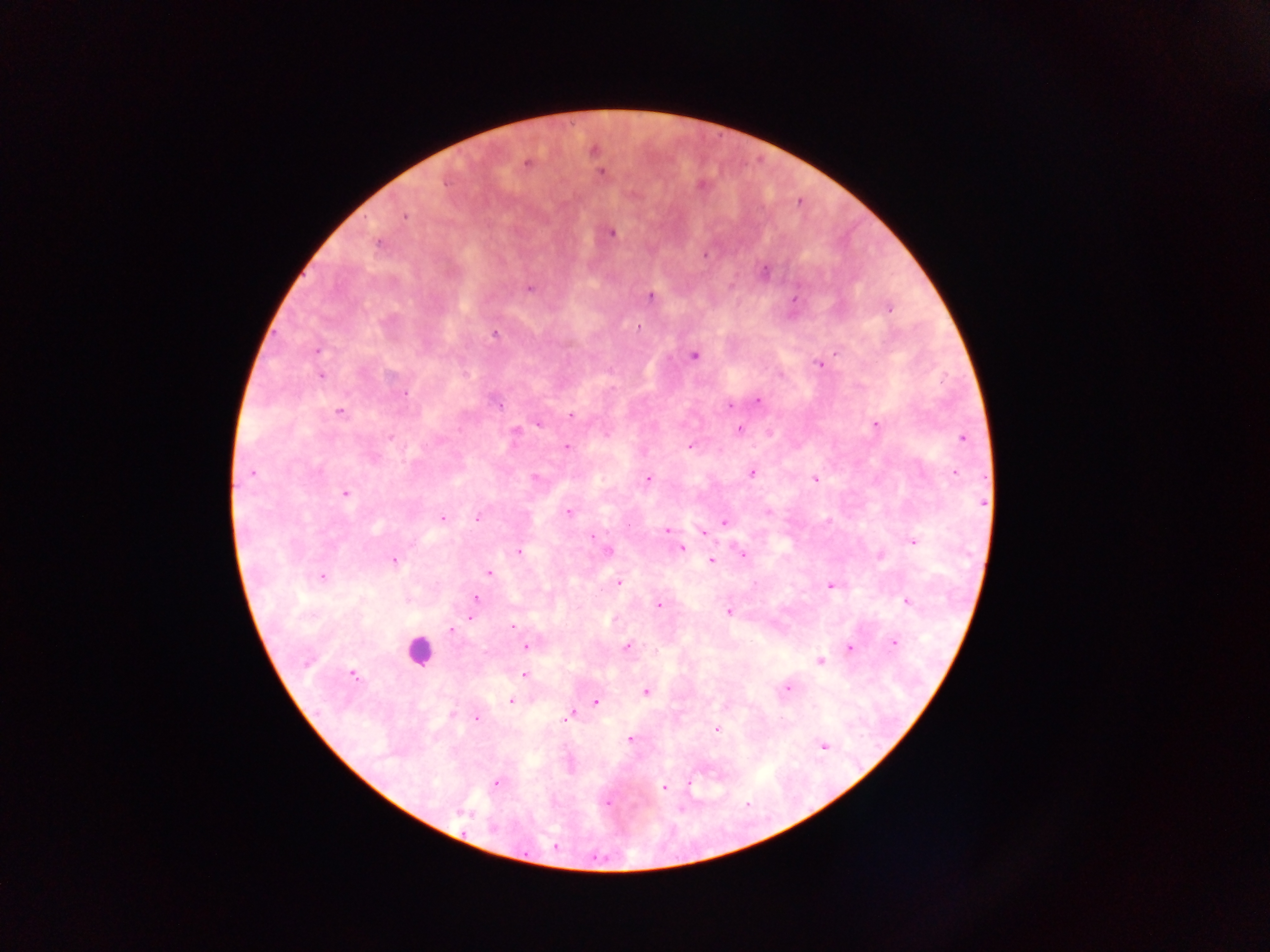
Approximate centers as {x, y} in pixels.
Summary:
  - Leukocyte locations: {420, 650}
  - Plasmodium parasite locations: {593, 150}, {527, 163}, {602, 174}, {405, 216}, {611, 233}, {377, 244}, {704, 255}, {765, 271}, {529, 288}, {650, 296}, {794, 299}, {890, 308}, {638, 327}, {495, 334}, {316, 350}, {837, 353}, {694, 355}, {826, 360}, {820, 364}, {320, 375}, {780, 375}, {404, 394}, {757, 401}, {498, 405}, {730, 406}, {339, 413}, {570, 415}, {538, 423}, {876, 425}, {739, 429}, {390, 437}, {962, 439}, {566, 446}, {690, 446}, {752, 473}, {251, 474}, {956, 474}, {535, 477}, {648, 479}, {815, 479}, {345, 494}, {568, 512}, {478, 517}, {443, 518}, {724, 522}, {667, 530}, {703, 532}, {592, 538}, {913, 542}, {682, 547}, {607, 551}, {520, 552}, {743, 555}, {394, 560}, {711, 561}, {489, 573}, {322, 577}, {618, 582}, {830, 586}, {476, 599}, {908, 602}, {658, 604}, {729, 612}, {471, 618}, {514, 626}, {451, 630}, {894, 643}, {627, 646}, {527, 647}, {849, 647}, {819, 661}, {306, 663}, {352, 674}, {524, 675}, {788, 688}, {645, 691}, {511, 702}, {595, 702}, {451, 714}, {568, 717}, {477, 719}, {716, 729}, {630, 739}, {824, 746}, {496, 783}, {689, 783}, {663, 787}, {607, 802}, {554, 846}
  - Field of view: single
  - Country: Ghana
  - Capture: mobile-phone photograph through a microscope
  - Image size: 1270×952 pixels
  - Preparation: thick blood smear